Locate every malaria parasite and every leukocyte.
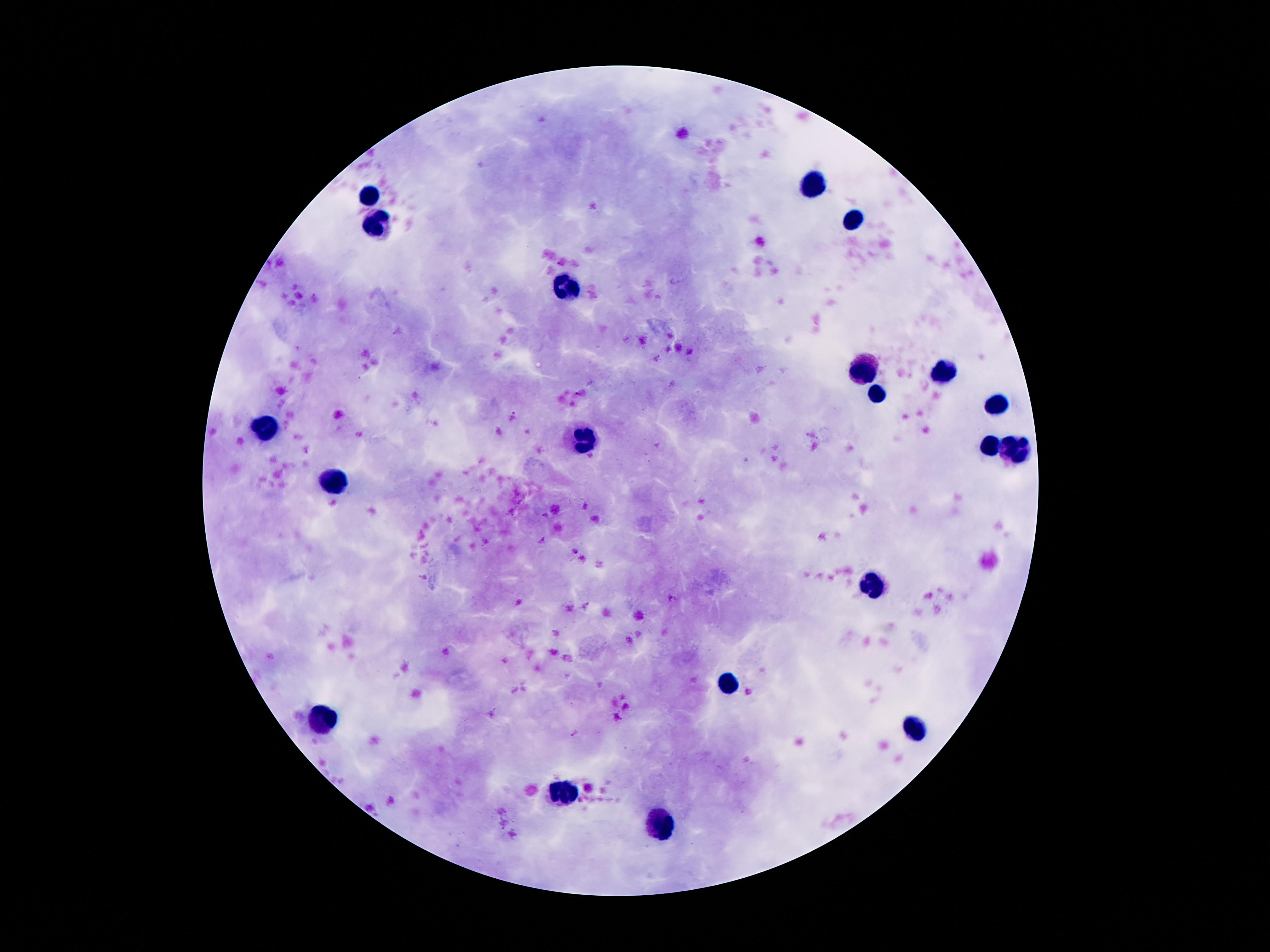

Approximate object centers, in pixels from the top-left corner.
Malaria parasites: (x=513, y=416), (x=544, y=515), (x=575, y=734).
Leukocytes: (x=813, y=187), (x=368, y=196), (x=850, y=224), (x=378, y=226), (x=569, y=282), (x=865, y=370), (x=942, y=375), (x=875, y=396), (x=996, y=406), (x=264, y=427), (x=583, y=436), (x=986, y=448), (x=1016, y=450), (x=326, y=481), (x=873, y=586), (x=729, y=685), (x=324, y=719), (x=917, y=729), (x=564, y=791), (x=662, y=821).

Summary:
  - Magnification: 100x
  - Capture: smartphone through the microscope eyepiece
  - Field of view: single
  - Image size: 1270×952 pixels
  - Preparation: thick peripheral-blood smear
  - Stain: Giemsa
  - Patient malaria status: infected with Plasmodium falciparum